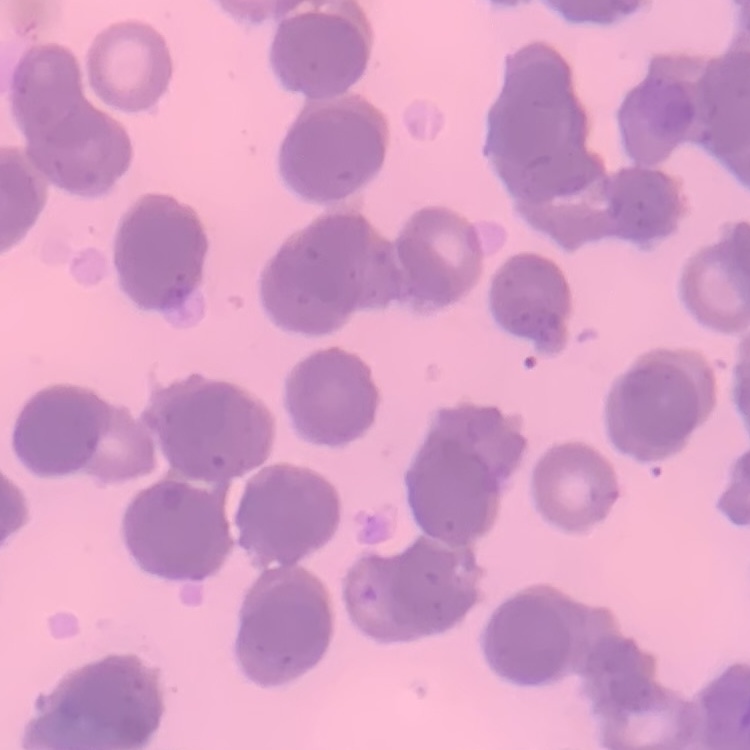
The red blood cells exhibit rouleaux formation. Field's or Giemsa stain. Thin blood smear. One tile cut from a larger photomicrograph.